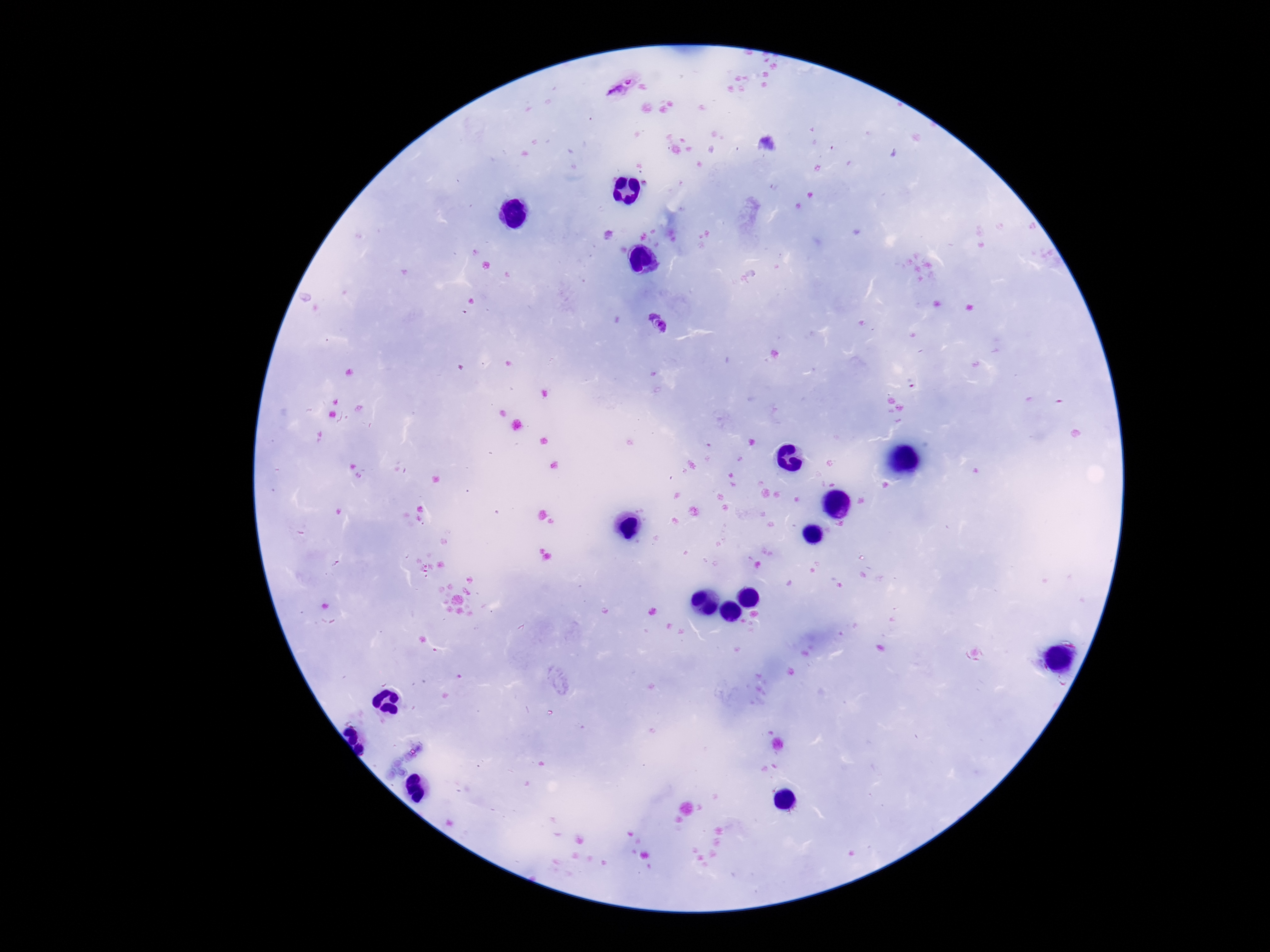
Approximate object centers, in pixels from the top-left corner. Plasmodium parasite locations: (x=623, y=87), (x=658, y=326). Giemsa stain. Photographed through the microscope eyepiece with a smartphone camera. One field from this slide. Thick blood smear. 100x magnification. Image is 1270×952 pixels. Patient malaria status: infected.